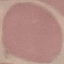
Summary:
  - Result: negative for malaria parasites
  - Preparation: thin blood smear
  - Image type: automatically extracted cell patch, resized to 64 × 64 pixels
  - Capture: smartphone through the microscope eyepiece
  - Stain: Giemsa